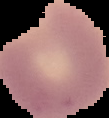

Summary:
  - Preparation: thin blood film
  - Image type: segmented cell region with the area outside set to black
  - Malaria status: parasitized
  - Image size: 109×118 pixels